Outline each blood parasite and name the species.
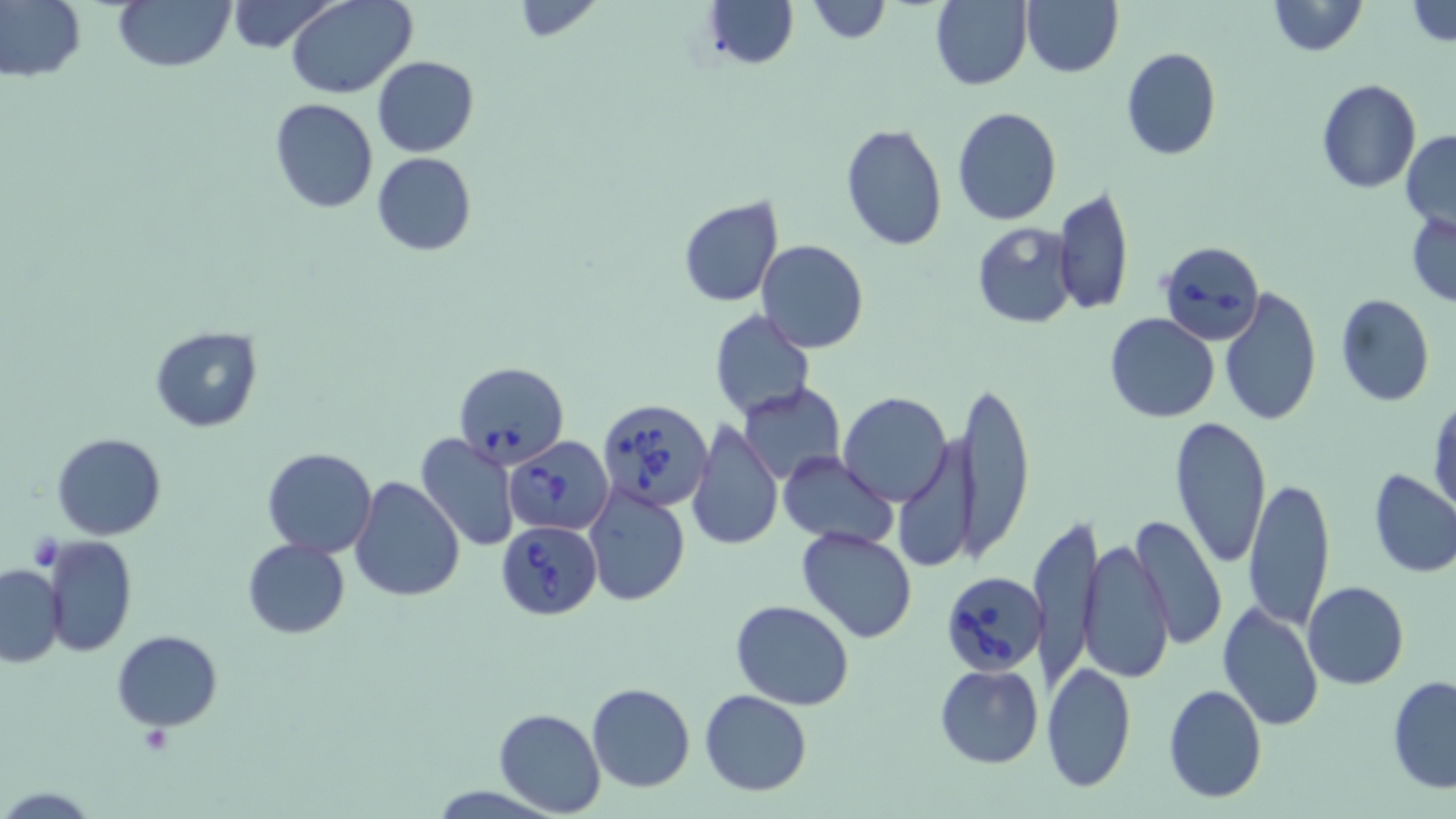
Approximate bounding boxes as [x1, y1, x2, y2] in pixels.
Babesia divergens-infected red blood cells: [1156, 240, 1264, 345], [453, 361, 569, 467], [596, 398, 715, 515], [504, 437, 613, 536], [497, 521, 602, 620], [941, 570, 1045, 675].
No Plasmodium falciparum, Plasmodium ovale, Plasmodium malariae, Plasmodium vivax, or Trypanosoma brucei observed.

Uninfected red blood cell locations: [114, 0, 234, 73], [224, 0, 339, 53], [285, 0, 417, 98], [702, 0, 798, 69], [804, 0, 892, 45], [928, 0, 1033, 90], [1021, 0, 1122, 78], [1266, 0, 1367, 56], [1405, 0, 1456, 49], [0, 1, 85, 83], [502, 2, 609, 41], [1121, 48, 1220, 161], [372, 55, 479, 158], [1315, 78, 1421, 195], [269, 98, 379, 215], [951, 106, 1062, 225], [840, 123, 948, 250], [1402, 129, 1456, 232], [371, 151, 477, 256], [1054, 185, 1134, 318], [678, 196, 784, 307], [1407, 213, 1456, 306], [970, 221, 1079, 329], [756, 240, 868, 352], [1218, 287, 1323, 428], [1335, 294, 1434, 406], [708, 310, 815, 422], [1103, 313, 1219, 423], [149, 324, 262, 431], [959, 378, 1035, 563], [739, 383, 846, 485], [838, 392, 953, 506], [1428, 396, 1456, 520], [1167, 416, 1272, 567], [686, 419, 783, 553], [896, 423, 982, 578], [51, 432, 167, 540], [414, 433, 521, 552], [262, 447, 378, 558], [779, 451, 898, 550], [1368, 468, 1456, 580], [1243, 476, 1335, 631], [351, 477, 464, 603], [584, 485, 692, 606], [1129, 512, 1227, 651], [1029, 513, 1101, 692], [796, 526, 920, 644], [41, 534, 136, 656], [1079, 537, 1174, 684], [242, 538, 350, 638], [0, 563, 66, 667], [1303, 581, 1409, 690], [731, 598, 855, 711], [1216, 599, 1324, 733], [111, 630, 222, 731], [1041, 661, 1137, 794], [934, 664, 1043, 768], [1387, 675, 1456, 794], [586, 683, 695, 793], [1162, 683, 1267, 802], [700, 690, 813, 796], [494, 708, 604, 816]. Slide-level diagnosis: Babesia divergens. Light microscopy. Captured at 1000x magnification. May-Grünwald-Giemsa stain. Single field of view. Image is 1456×819 pixels. Thin blood smear.